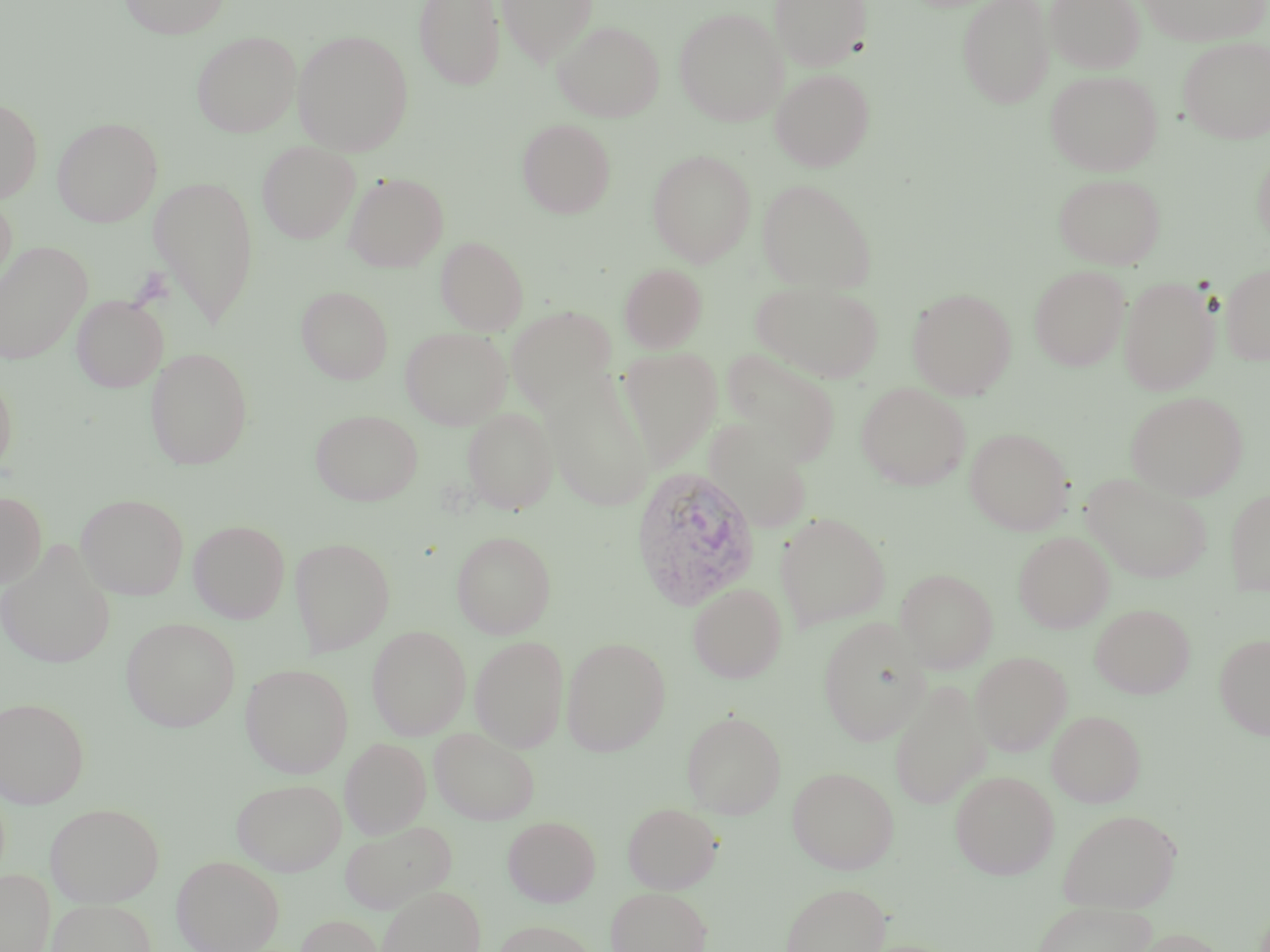

Summary:
  - Coordinate format: approximate bounding boxes as (x1,y1)-(x2,y2) corner pairs in pixels
  - Plasmodium vivax-infected red blood cell locations: (629,465)-(762,611)
  - Uninfected red blood cell locations: (118,0)-(230,39), (412,0)-(505,91), (497,0)-(597,65), (770,0)-(864,70), (957,0)-(1054,109), (1046,0)-(1145,73), (1139,0)-(1269,47), (674,8)-(787,126), (552,20)-(664,122), (191,30)-(302,137), (292,30)-(414,155), (1179,37)-(1270,143), (771,68)-(871,172), (1045,69)-(1163,176), (0,97)-(43,204), (53,117)-(163,227), (517,118)-(617,219), (257,141)-(361,244), (1253,146)-(1270,247), (647,149)-(755,267), (344,172)-(448,272), (1053,172)-(1165,269), (149,175)-(260,327), (756,178)-(877,294), (0,194)-(17,298), (436,236)-(529,335), (0,241)-(92,364), (619,263)-(707,352), (1220,263)-(1270,365), (1029,265)-(1130,371), (1119,276)-(1219,395), (750,279)-(885,383), (296,285)-(394,384), (908,288)-(1016,399), (72,294)-(167,392), (507,306)-(616,410), (400,326)-(511,429), (146,347)-(254,470), (618,347)-(723,468), (720,347)-(841,465), (0,370)-(17,480), (541,375)-(656,511), (856,382)-(971,490), (1126,392)-(1248,500), (463,407)-(557,515), (310,408)-(423,506), (710,426)-(816,535), (965,428)-(1073,534), (1081,474)-(1213,584), (1225,488)-(1270,594), (0,491)-(46,589), (77,493)-(189,600), (775,511)-(891,631), (189,520)-(290,622), (451,530)-(556,638), (1014,531)-(1114,633), (289,537)-(395,654), (0,542)-(116,668), (895,568)-(998,672), (688,583)-(788,684), (1090,604)-(1194,698), (121,617)-(241,732), (818,619)-(932,745), (367,626)-(471,740), (1214,633)-(1270,740), (469,635)-(569,752), (561,636)-(671,757), (971,652)-(1072,755), (241,663)-(354,778), (888,680)-(990,810), (1,696)-(89,808), (1047,709)-(1146,807), (681,710)-(787,819), (429,727)-(540,825), (340,737)-(431,838), (787,766)-(900,874), (950,771)-(1059,879), (231,777)-(346,876), (45,802)-(165,907), (622,802)-(723,893), (1058,808)-(1182,912), (502,816)-(601,907), (339,819)-(457,915), (172,855)-(284,952), (0,869)-(54,952), (780,882)-(891,952), (375,885)-(487,952), (606,886)-(712,952), (47,899)-(156,952), (1031,899)-(1157,952), (295,914)-(385,952), (492,920)-(600,952), (1130,927)-(1229,952)
  - Slide-level diagnosis: Plasmodium vivax
  - Modality: optical microscopy
  - Preparation: thin blood smear
  - Stain: May-Grünwald-Giemsa
  - Field of view: single
  - Magnification: 1000x
  - Image size: 1270×952 pixels